Comment on the morphology of the erythrocytes.
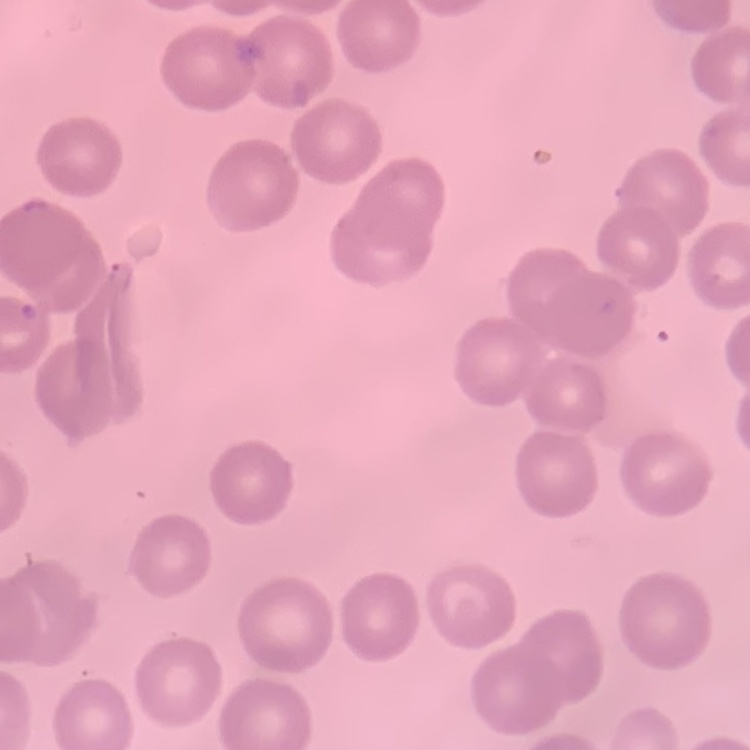

They show no rouleaux formation.

Summary:
  - Preparation: thin blood film
  - Stain: Field's or Giemsa
  - Image type: one tile cut from a larger photomicrograph